Assess this cell for malaria.
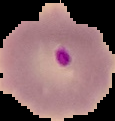

It is parasitized.

image size = 115×121 pixels
preparation = thin blood smear
image type = segmented cell region on a black background